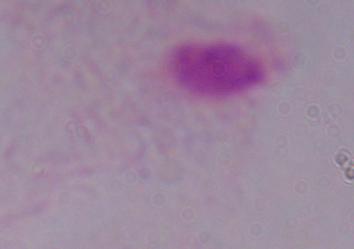
magnification = 1000x
identification = trichomonad
modality = micrograph